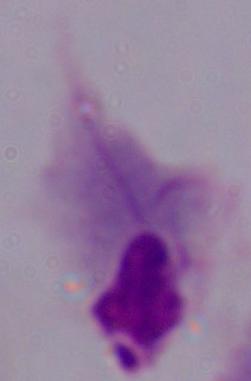
Summary:
  - Modality: photomicrograph
  - Magnification: 1000x
  - Identification: trichomonad